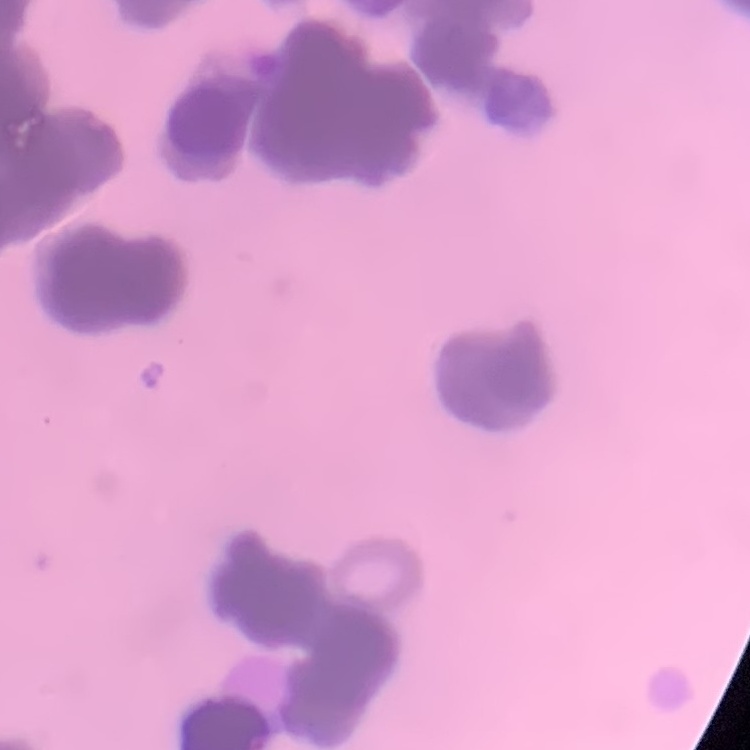

red_blood_cell_morphology: rouleaux formation
preparation: thin peripheral smear
image_type: one tile cut from a larger photomicrograph
stain: Field's or Giemsa